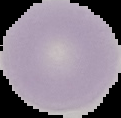
From a thin blood film. Image is 121×118 pixels. Result: no malaria parasites seen. The area outside the segmented cell region is set to black.